Evaluate for Plasmodium parasites.
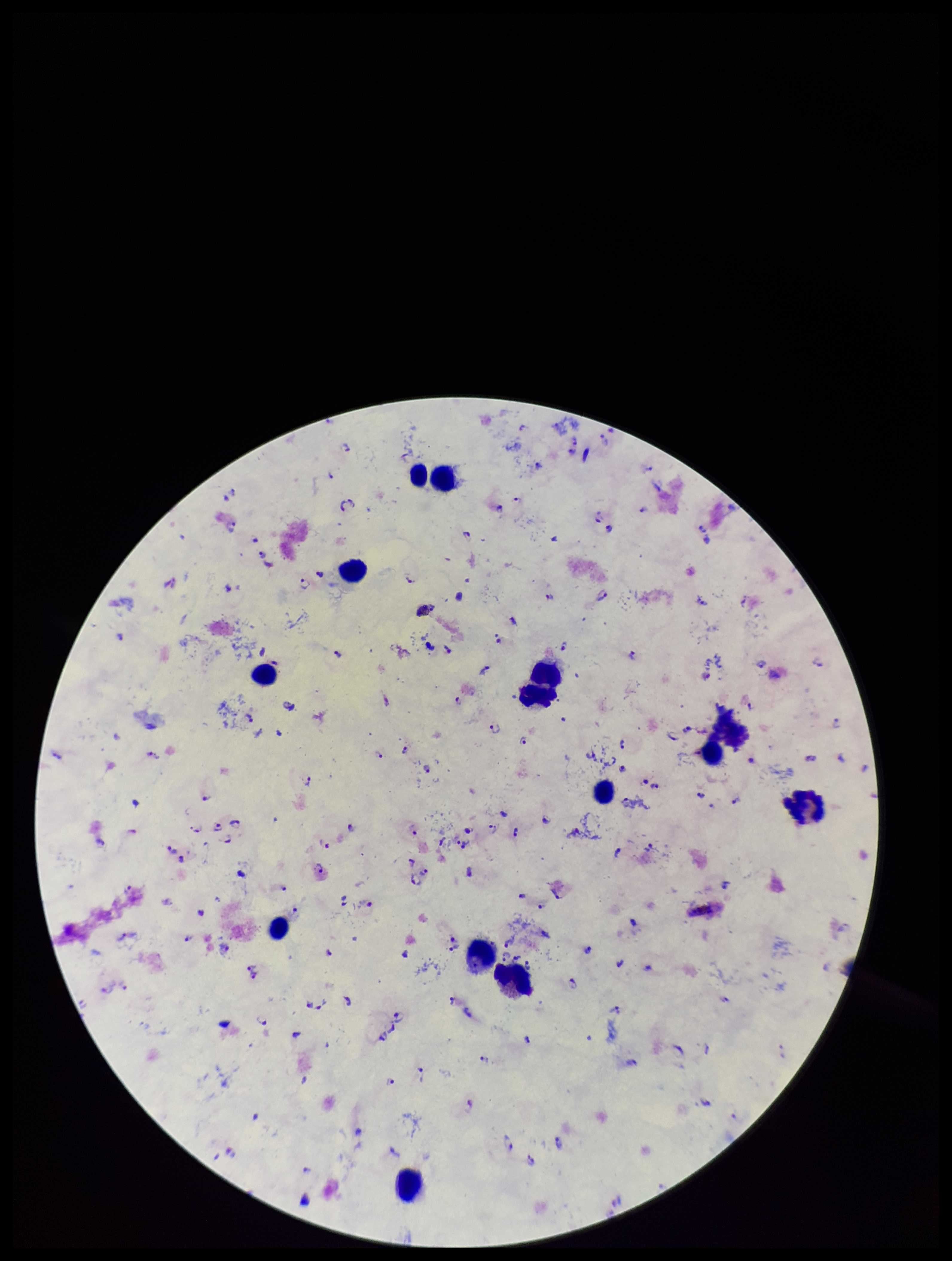

Identified.

Summary:
  - Species reported for this patient: Plasmodium falciparum
  - Capture: smartphone photograph through the microscope eyepiece
  - Field of view: one from this slide
  - Patient malaria status: infected
  - Image size: 952×1261 pixels
  - Stain: Giemsa
  - Preparation: thick smear
  - Leukocyte count: 12
  - Parasite count: 109